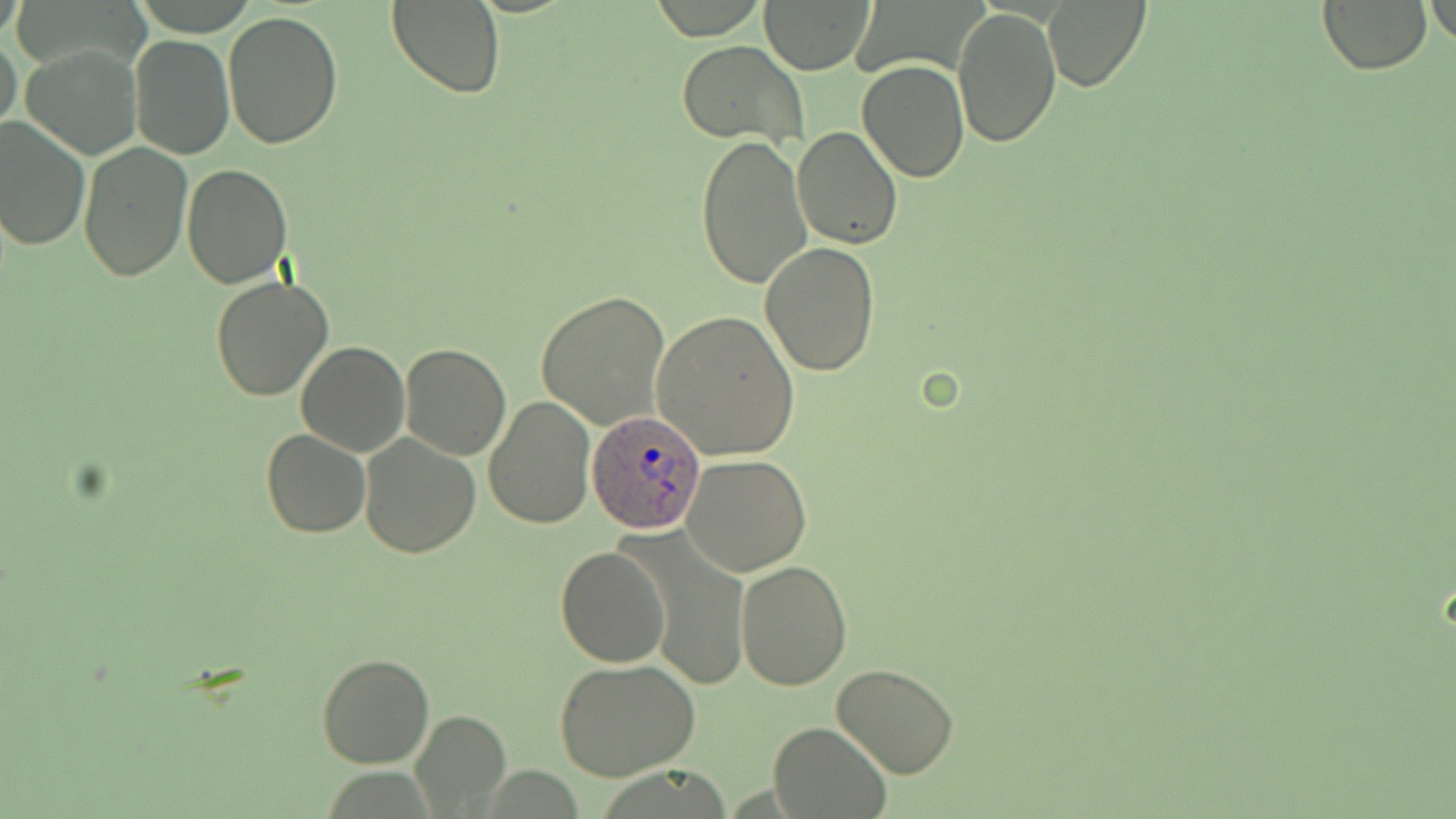
Approximate bounding boxes as [x1, y1, x2, y2] in pixels. Uninfected red blood cell locations: [759, 0, 875, 74], [1043, 0, 1152, 93], [1427, 0, 1455, 53], [387, 1, 507, 98], [1319, 1, 1432, 75], [954, 7, 1060, 148], [222, 10, 343, 149], [0, 32, 23, 140], [129, 35, 236, 159], [678, 40, 806, 147], [19, 43, 143, 161], [857, 62, 970, 183], [0, 116, 90, 252], [791, 124, 903, 248], [694, 134, 812, 291], [78, 144, 194, 283], [182, 165, 292, 289], [759, 242, 883, 376], [211, 276, 333, 401], [537, 290, 671, 432], [650, 309, 800, 460], [296, 340, 409, 457], [400, 344, 512, 460], [484, 393, 595, 528], [261, 429, 371, 539], [358, 432, 483, 557], [682, 454, 813, 575], [629, 530, 752, 690], [556, 543, 671, 666], [735, 558, 853, 690], [317, 652, 433, 768], [554, 660, 701, 782], [831, 663, 959, 779], [412, 711, 509, 811], [768, 720, 891, 818]. Plasmodium ovale-infected red blood cell locations: [586, 407, 704, 533]. Slide-level diagnosis: Plasmodium ovale. Thin blood film. Captured at 1000x magnification. Image is 1456×819 pixels. May-Grünwald-Giemsa stain. Single field of view. Optical microscopy.